Give the extent of all Plasmodium vivax-infected red blood cells.
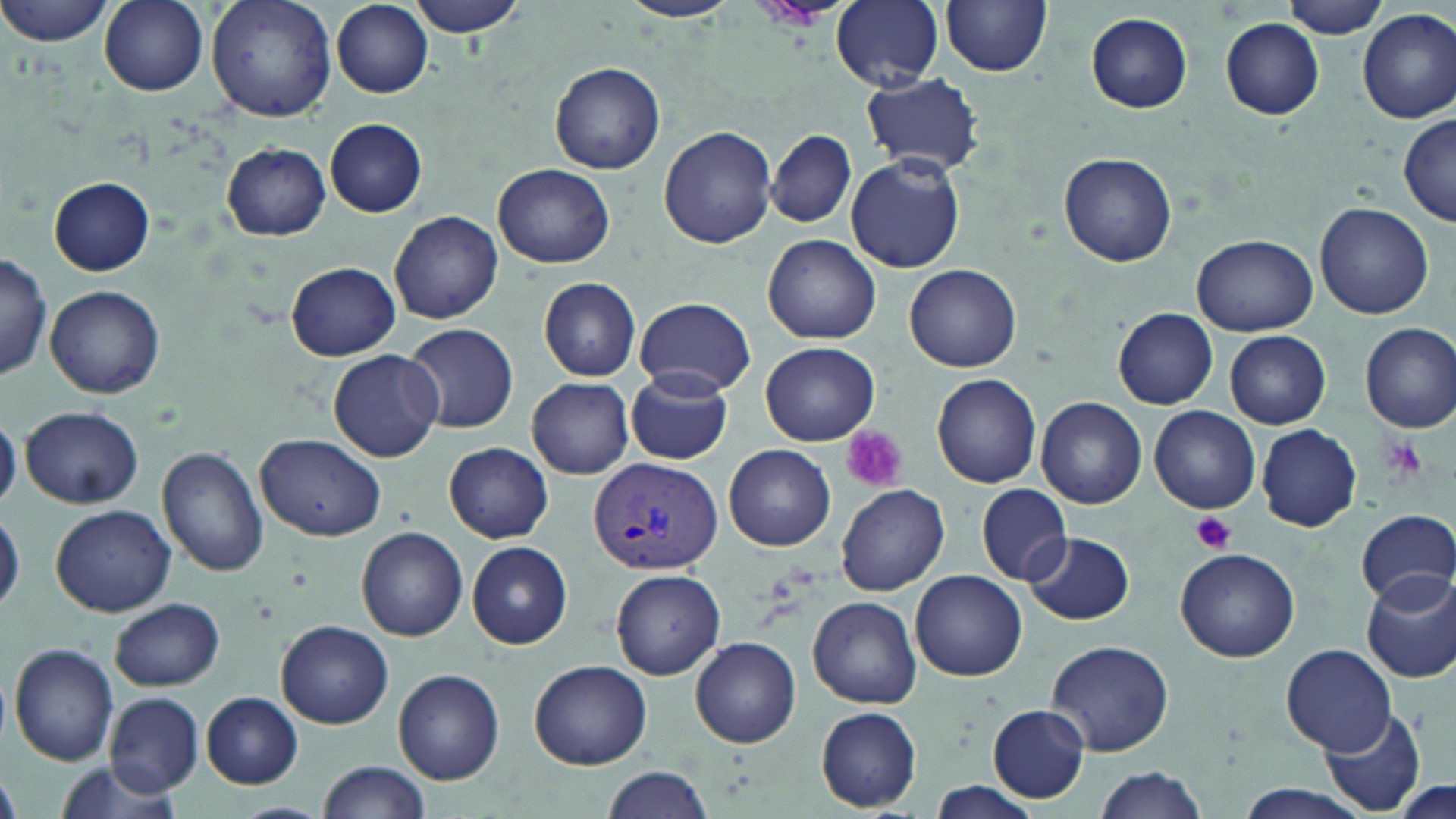
Approximate bounding boxes as (x1,y1)-(x2,y2) corner pairs in pixels.
Plasmodium vivax-infected red blood cells: (588,455)-(722,575).

{
  "slide_level_diagnosis": "Plasmodium vivax",
  "stain": "May-Grünwald-Giemsa",
  "uninfected_red_blood_cell_locations": "approximate bounding boxes as (x1,y1)-(x2,y2) corner pairs in pixels: (1,0)-(117,46), (99,0)-(208,94), (206,0)-(337,122), (406,0)-(530,37), (619,0)-(739,24), (832,0)-(944,89), (1280,0)-(1392,38), (940,1)-(1054,76), (332,3)-(434,99), (1358,9)-(1456,123), (1084,12)-(1193,112), (1219,18)-(1325,120), (550,62)-(666,175), (859,72)-(986,176), (1399,111)-(1456,225), (325,117)-(427,216), (659,125)-(776,248), (767,129)-(857,229), (221,143)-(331,240), (1058,152)-(1175,267), (846,154)-(965,273), (493,163)-(615,270), (49,178)-(154,276), (1314,202)-(1433,318), (390,211)-(503,325), (763,234)-(883,344), (1194,234)-(1316,336), (0,251)-(52,381), (285,261)-(399,360), (904,263)-(1022,372), (538,277)-(642,381), (45,285)-(164,398), (633,297)-(757,398), (1115,309)-(1217,411), (1360,322)-(1456,434), (404,323)-(519,433), (1225,330)-(1331,428), (761,342)-(879,445), (328,349)-(445,461), (625,369)-(733,464), (932,373)-(1043,489), (527,378)-(634,478), (1035,396)-(1148,509), (21,405)-(142,508), (1150,406)-(1260,512), (0,416)-(22,511), (1257,424)-(1360,531), (256,435)-(385,543), (444,442)-(553,543), (723,444)-(836,551), (157,446)-(269,578), (836,483)-(949,596), (975,484)-(1074,584), (51,504)-(176,618), (0,508)-(23,617), (1355,512)-(1455,606), (356,528)-(468,641), (1023,531)-(1136,626), (465,541)-(573,650), (1175,546)-(1300,662), (1360,568)-(1456,683), (610,569)-(725,679), (910,570)-(1028,681), (808,596)-(921,708), (112,598)-(224,691), (279,621)-(392,727), (689,637)-(801,747), (1045,640)-(1174,757), (9,643)-(119,767), (1281,644)-(1395,755), (529,659)-(653,768), (393,668)-(506,786), (104,692)-(206,797), (203,693)-(303,789), (988,705)-(1090,803), (1320,706)-(1428,815), (816,708)-(921,812), (318,760)-(431,817), (51,762)-(185,819), (602,765)-(716,819), (1090,766)-(1209,819), (1,773)-(20,819), (1386,777)-(1456,819), (928,781)-(1043,817), (1236,786)-(1362,819), (229,801)-(336,818)",
  "magnification": "1000x",
  "image_size": "1456×819 pixels",
  "field_of_view": "single",
  "modality": "optical microscopy",
  "platelet_locations": "approximate bounding boxes as (x1,y1)-(x2,y2) corner pairs in pixels: (839,426)-(906,492), (1193,512)-(1235,552)",
  "preparation": "thin blood smear"
}